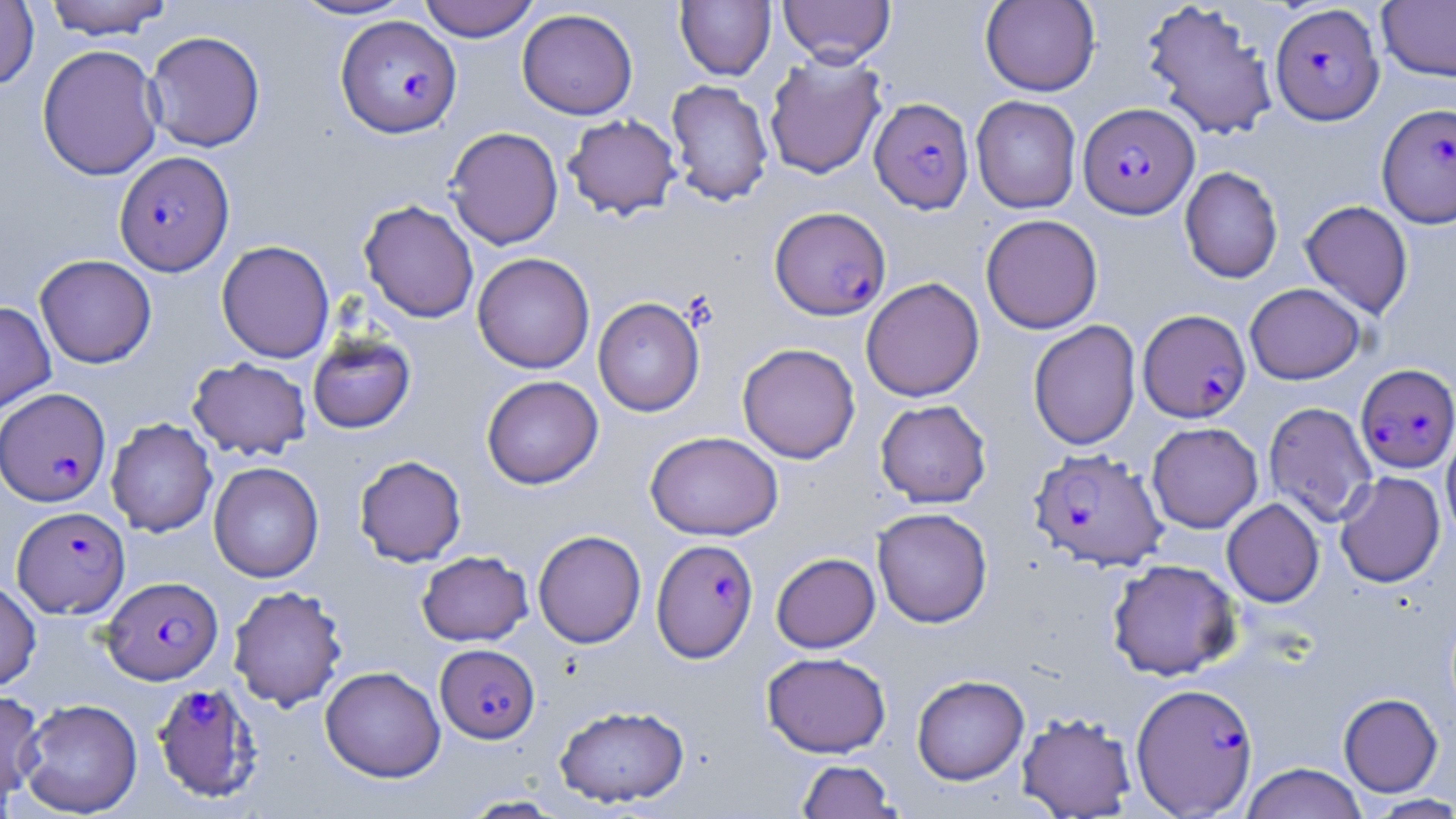

Approximate bounding boxes as (x1,y1)-(x2,y2) corner pairs in pixels. Uninfected red blood cell locations: (43,0)-(175,39), (287,0)-(419,21), (417,0)-(540,42), (778,0)-(895,66), (980,0)-(1100,96), (0,1)-(39,89), (675,1)-(776,81), (1141,1)-(1279,141), (1377,1)-(1456,82), (517,8)-(638,120), (144,30)-(266,152), (36,44)-(164,180), (764,53)-(887,180), (665,79)-(774,206), (971,96)-(1081,213), (563,114)-(681,219), (445,127)-(563,249), (1180,166)-(1283,284), (359,200)-(479,323), (1299,200)-(1414,319), (980,214)-(1103,334), (216,240)-(335,363), (472,252)-(595,374), (34,254)-(157,368), (860,277)-(984,402), (1244,283)-(1366,384), (593,297)-(705,416), (0,301)-(56,414), (1028,320)-(1141,451), (307,333)-(416,434), (737,342)-(860,464), (187,357)-(312,459), (481,375)-(603,489), (875,399)-(991,507), (1263,402)-(1377,526), (106,417)-(217,537), (1147,422)-(1263,533), (1441,427)-(1456,546), (645,431)-(783,540), (354,455)-(467,566), (208,461)-(324,582), (1334,471)-(1445,587), (1222,498)-(1325,607), (872,507)-(993,628), (533,530)-(646,648), (416,550)-(533,646), (771,552)-(880,653), (1107,558)-(1241,680), (0,576)-(41,692), (228,585)-(347,711), (761,651)-(892,757), (320,666)-(445,782), (912,674)-(1029,785), (0,687)-(44,807), (1338,692)-(1443,796), (17,698)-(143,817), (554,703)-(690,808), (1017,711)-(1137,818), (796,759)-(901,818), (1240,762)-(1367,819), (1363,794)-(1456,818), (459,795)-(567,818). Plasmodium falciparum-infected red blood cell locations: (1270,3)-(1384,125), (335,15)-(462,137), (869,97)-(974,214), (1078,102)-(1199,218), (1377,102)-(1456,227), (114,151)-(235,276), (769,206)-(891,320), (1138,309)-(1251,422), (1355,363)-(1456,473), (1,388)-(112,507), (1029,448)-(1166,571), (12,506)-(130,619), (651,538)-(758,663), (102,576)-(223,685), (435,644)-(540,743), (151,681)-(264,803), (1131,682)-(1259,816). Slide-level diagnosis: Plasmodium falciparum. Captured at 1000x magnification. Thin blood smear. One field of a larger specimen. May-Grünwald-Giemsa-stained preparation. Light microscopy. Image is 1456×819 pixels.